Classify this cell by malaria status.
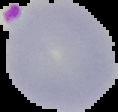
It is parasitized.

Image is 118×112 pixels. Cell region segmented out of the field of view; the surrounding area is masked to black. From a thin blood film.